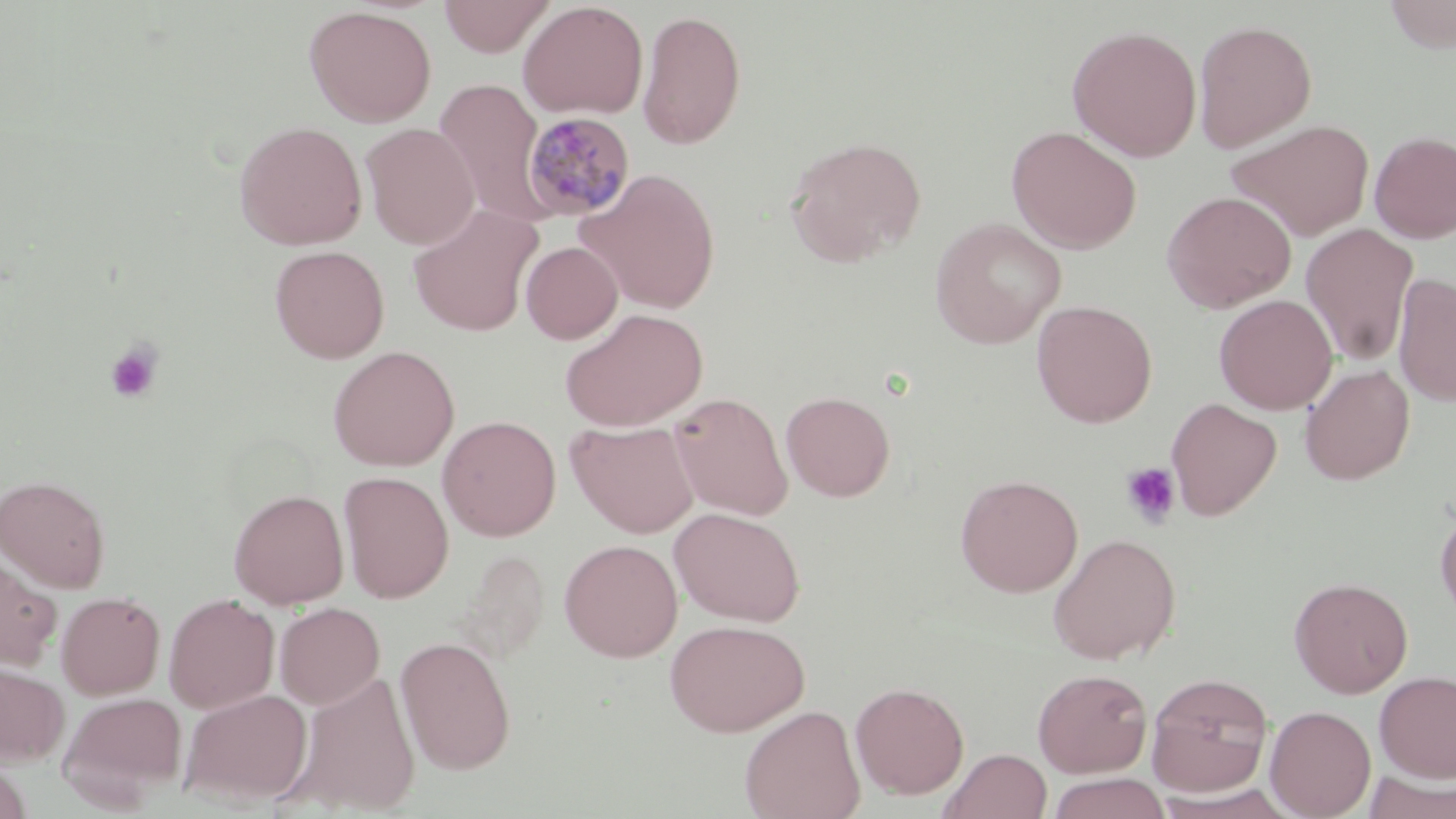 Approximate bounding boxes as named x1/y1/x2/y2 corners in pixels. Plasmodium malariae-infected red blood cell locations: (x1=519, y1=111, x2=636, y2=221). Uninfected red blood cell locations: (x1=438, y1=0, x2=556, y2=57), (x1=1383, y1=0, x2=1456, y2=53), (x1=518, y1=1, x2=648, y2=119), (x1=303, y1=5, x2=438, y2=127), (x1=637, y1=8, x2=746, y2=151), (x1=1193, y1=19, x2=1317, y2=152), (x1=1066, y1=25, x2=1202, y2=162), (x1=433, y1=77, x2=552, y2=225), (x1=1226, y1=118, x2=1375, y2=242), (x1=234, y1=120, x2=368, y2=250), (x1=361, y1=122, x2=480, y2=250), (x1=1006, y1=126, x2=1142, y2=253), (x1=1369, y1=131, x2=1456, y2=244), (x1=785, y1=136, x2=927, y2=267), (x1=577, y1=168, x2=721, y2=315), (x1=1162, y1=190, x2=1297, y2=313), (x1=408, y1=204, x2=543, y2=337), (x1=930, y1=217, x2=1066, y2=348), (x1=1300, y1=223, x2=1420, y2=365), (x1=521, y1=241, x2=623, y2=344), (x1=269, y1=245, x2=390, y2=363), (x1=1393, y1=272, x2=1456, y2=408), (x1=1214, y1=293, x2=1337, y2=415), (x1=1031, y1=299, x2=1157, y2=428), (x1=559, y1=307, x2=707, y2=431), (x1=327, y1=345, x2=460, y2=471), (x1=1300, y1=364, x2=1415, y2=485), (x1=781, y1=391, x2=894, y2=502), (x1=669, y1=392, x2=793, y2=521), (x1=1166, y1=397, x2=1282, y2=520), (x1=437, y1=415, x2=561, y2=541), (x1=566, y1=420, x2=701, y2=538), (x1=338, y1=470, x2=454, y2=603), (x1=0, y1=474, x2=112, y2=593), (x1=955, y1=474, x2=1083, y2=597), (x1=228, y1=487, x2=349, y2=609), (x1=1434, y1=503, x2=1456, y2=626), (x1=670, y1=506, x2=806, y2=627), (x1=1047, y1=533, x2=1181, y2=664), (x1=559, y1=539, x2=683, y2=662), (x1=454, y1=549, x2=549, y2=665), (x1=0, y1=554, x2=63, y2=670), (x1=1289, y1=576, x2=1413, y2=698), (x1=56, y1=590, x2=166, y2=699), (x1=163, y1=593, x2=280, y2=714), (x1=274, y1=602, x2=385, y2=710), (x1=664, y1=618, x2=810, y2=736), (x1=395, y1=636, x2=516, y2=775), (x1=0, y1=661, x2=70, y2=766), (x1=1032, y1=668, x2=1152, y2=778), (x1=287, y1=670, x2=422, y2=816), (x1=1374, y1=671, x2=1456, y2=783), (x1=1146, y1=672, x2=1274, y2=798), (x1=850, y1=681, x2=969, y2=799), (x1=180, y1=689, x2=313, y2=808), (x1=59, y1=691, x2=186, y2=806), (x1=739, y1=705, x2=866, y2=819), (x1=1265, y1=705, x2=1376, y2=819), (x1=940, y1=748, x2=1052, y2=819), (x1=0, y1=758, x2=33, y2=819), (x1=1362, y1=772, x2=1456, y2=819), (x1=1046, y1=773, x2=1172, y2=819). Platelet locations: (x1=105, y1=341, x2=163, y2=404), (x1=1120, y1=462, x2=1182, y2=528). Slide-level diagnosis: Plasmodium malariae. Thin blood smear. May-Grünwald-Giemsa-stained preparation. Image is 1456×819 pixels. Captured at 1000x magnification. One field of a larger specimen. Light microscopy.